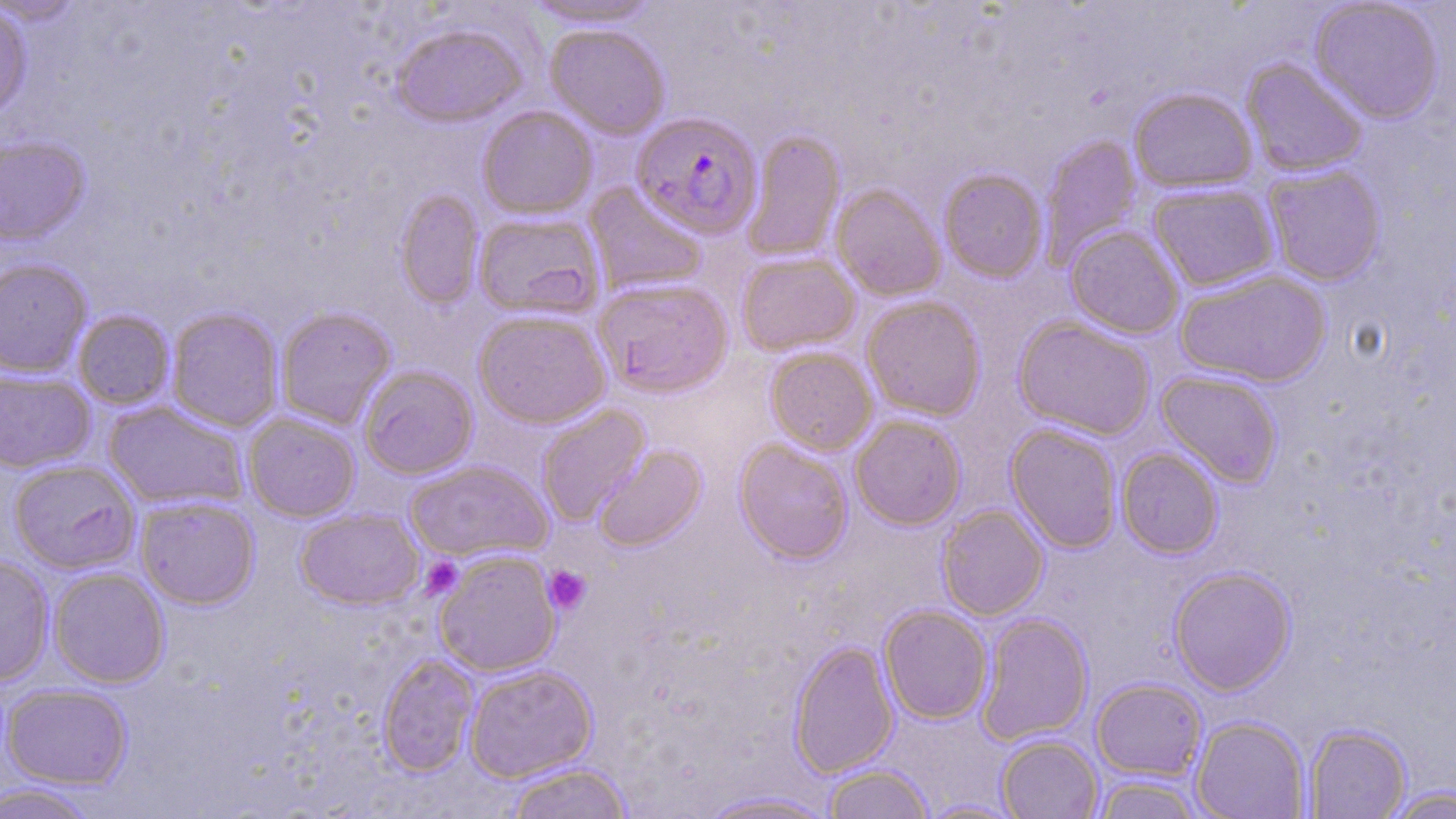

slide-level diagnosis = Plasmodium falciparum
magnification = 1000x
stain = May-Grünwald-Giemsa
platelet locations = approximate bounding boxes as named x1/y1/x2/y2 corners in pixels: (x1=421, y1=556, x2=464, y2=598), (x1=543, y1=565, x2=592, y2=615)
modality = light microscopy
uninfected red blood cell locations = approximate bounding boxes as named x1/y1/x2/y2 corners in pixels: (x1=0, y1=0, x2=85, y2=25), (x1=1308, y1=0, x2=1445, y2=125), (x1=522, y1=1, x2=667, y2=28), (x1=0, y1=3, x2=34, y2=122), (x1=544, y1=23, x2=670, y2=139), (x1=390, y1=24, x2=528, y2=128), (x1=1240, y1=58, x2=1368, y2=177), (x1=1128, y1=87, x2=1258, y2=193), (x1=477, y1=106, x2=598, y2=220), (x1=741, y1=129, x2=846, y2=262), (x1=1039, y1=134, x2=1142, y2=266), (x1=0, y1=136, x2=91, y2=246), (x1=1263, y1=164, x2=1386, y2=286), (x1=938, y1=169, x2=1048, y2=283), (x1=584, y1=181, x2=708, y2=296), (x1=1148, y1=183, x2=1279, y2=291), (x1=831, y1=184, x2=946, y2=301), (x1=394, y1=188, x2=484, y2=310), (x1=472, y1=211, x2=605, y2=321), (x1=1065, y1=226, x2=1184, y2=339), (x1=736, y1=251, x2=860, y2=357), (x1=0, y1=258, x2=92, y2=378), (x1=1175, y1=269, x2=1332, y2=387), (x1=593, y1=277, x2=734, y2=398), (x1=861, y1=296, x2=986, y2=421), (x1=166, y1=306, x2=284, y2=432), (x1=275, y1=306, x2=396, y2=429), (x1=473, y1=309, x2=611, y2=428), (x1=72, y1=310, x2=175, y2=410), (x1=1012, y1=316, x2=1156, y2=440), (x1=765, y1=348, x2=877, y2=455), (x1=359, y1=365, x2=478, y2=479), (x1=0, y1=368, x2=96, y2=473), (x1=1156, y1=370, x2=1283, y2=488), (x1=103, y1=400, x2=248, y2=511), (x1=536, y1=404, x2=651, y2=526), (x1=243, y1=412, x2=361, y2=522), (x1=850, y1=414, x2=967, y2=530), (x1=1006, y1=423, x2=1123, y2=553), (x1=734, y1=438, x2=854, y2=564), (x1=594, y1=443, x2=707, y2=552), (x1=1117, y1=447, x2=1224, y2=558), (x1=7, y1=459, x2=141, y2=574), (x1=404, y1=459, x2=553, y2=562), (x1=135, y1=495, x2=260, y2=609), (x1=936, y1=504, x2=1049, y2=620), (x1=295, y1=508, x2=424, y2=610), (x1=433, y1=550, x2=561, y2=677), (x1=0, y1=554, x2=54, y2=686), (x1=1169, y1=566, x2=1296, y2=696), (x1=49, y1=567, x2=169, y2=688), (x1=879, y1=604, x2=993, y2=724), (x1=976, y1=613, x2=1093, y2=745), (x1=788, y1=640, x2=900, y2=777), (x1=378, y1=653, x2=479, y2=776), (x1=463, y1=665, x2=597, y2=782), (x1=1091, y1=678, x2=1207, y2=781), (x1=2, y1=684, x2=134, y2=789), (x1=1191, y1=716, x2=1310, y2=819), (x1=1303, y1=724, x2=1412, y2=818), (x1=997, y1=734, x2=1103, y2=819), (x1=504, y1=762, x2=633, y2=819), (x1=822, y1=764, x2=934, y2=819), (x1=1090, y1=776, x2=1207, y2=819), (x1=0, y1=782, x2=99, y2=819), (x1=1382, y1=786, x2=1456, y2=818), (x1=693, y1=790, x2=844, y2=818), (x1=917, y1=798, x2=1028, y2=819)
preparation = thin blood film
image size = 1456×819 pixels
field of view = single
Plasmodium falciparum-infected red blood cell locations = approximate bounding boxes as named x1/y1/x2/y2 corners in pixels: (x1=631, y1=111, x2=763, y2=240)